Describe the morphology of the erythrocytes.
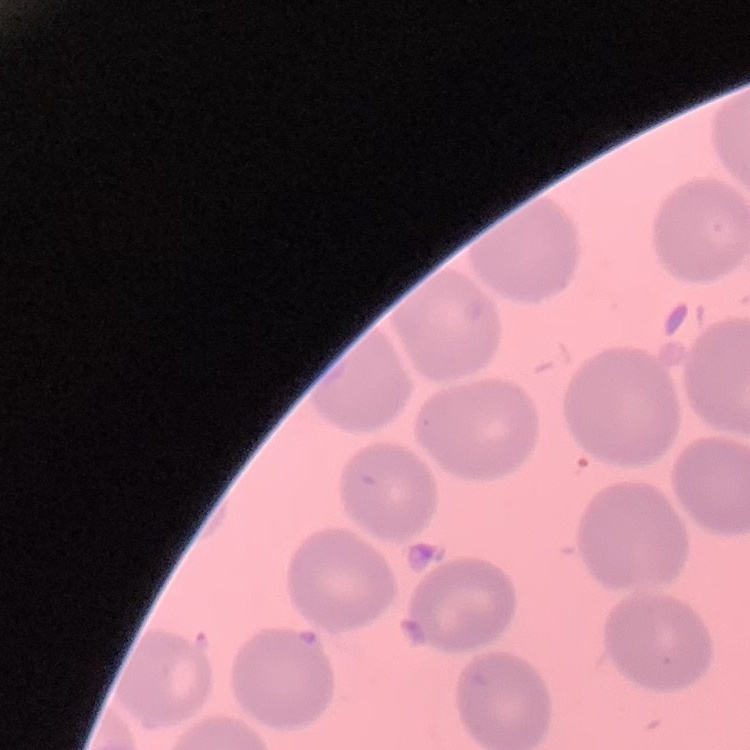
They show no rouleaux formation.

{
  "stain": "Field's or Giemsa",
  "preparation": "thin peripheral smear",
  "image_type": "one tile cut from a larger photomicrograph"
}